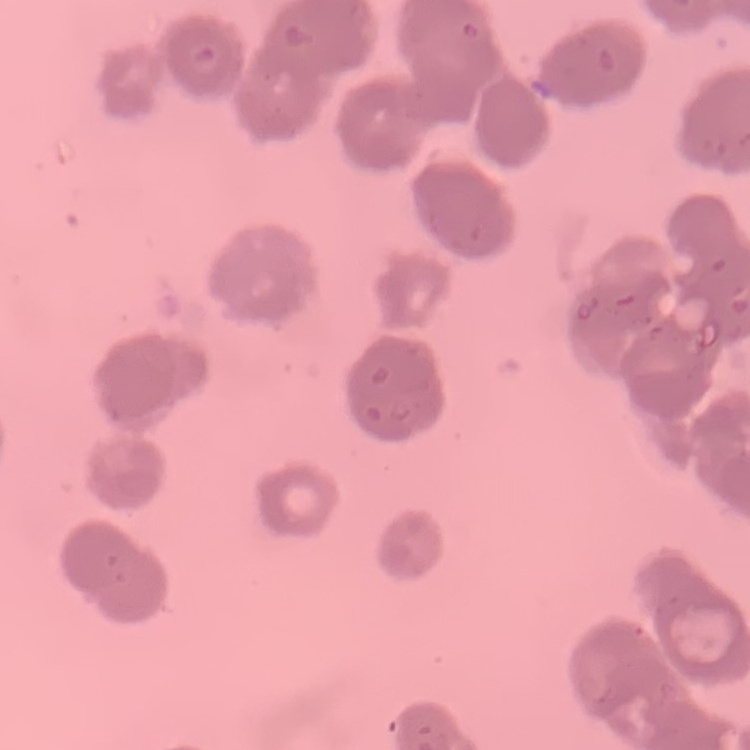

red blood cell morphology = rouleaux formation
preparation = thin peripheral smear
stain = Field's or Giemsa
image type = square crop of a larger photomicrograph